Assess the morphology of the erythrocytes.
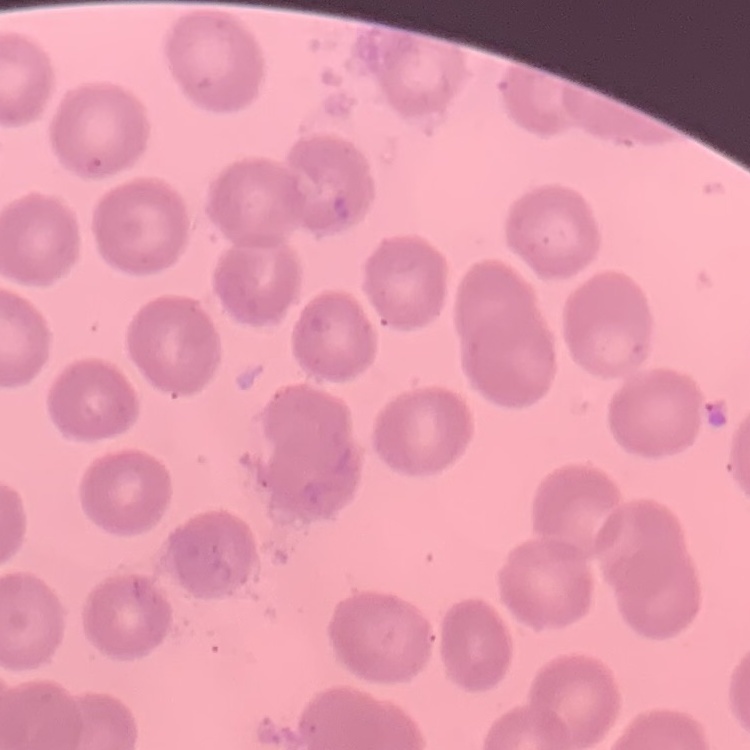
No rouleaux formation.

stain = Field's or Giemsa
image type = square crop of a larger photomicrograph
preparation = thin peripheral smear